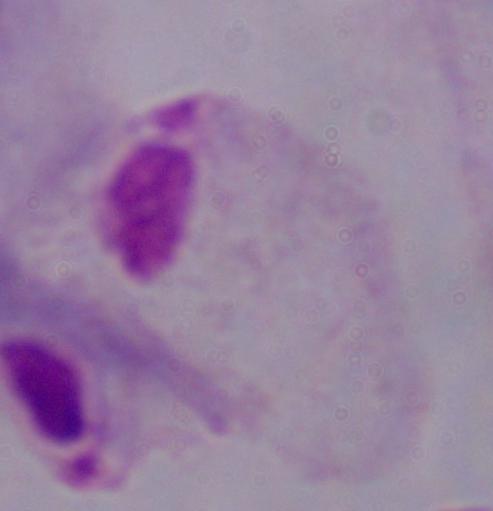

Summary:
  - Magnification: 1000x
  - Modality: photomicrograph
  - Identification: trichomonad